Locate every blood parasite and identify its species.
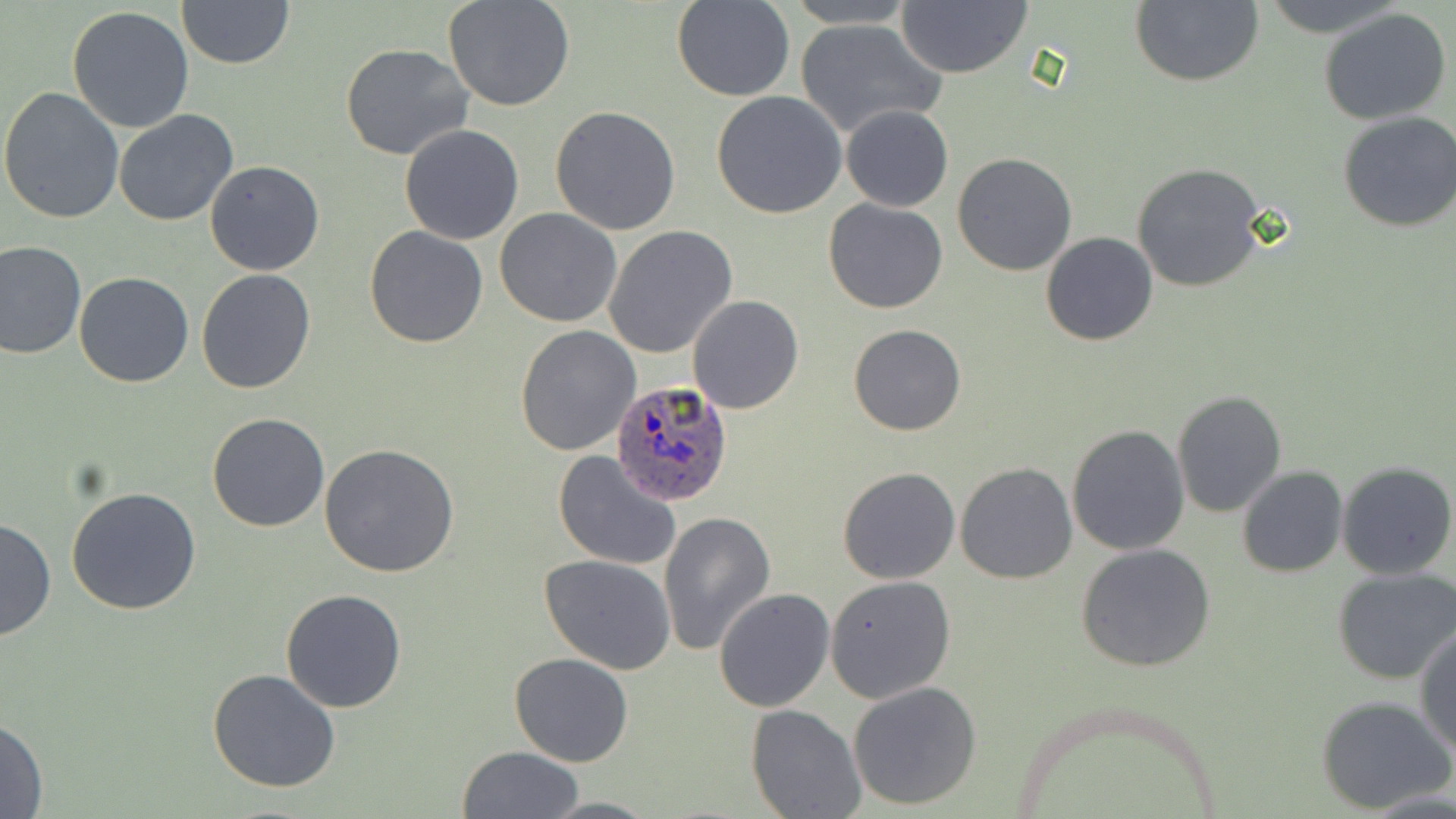

Approximate bounding boxes as (x1, y1, x2, y2) in pixels.
Plasmodium ovale-infected red blood cells: (610, 381, 732, 507).
No Plasmodium falciparum, Plasmodium malariae, Plasmodium vivax, Babesia divergens, or Trypanosoma brucei observed.

slide_level_diagnosis: Plasmodium ovale
magnification: 1000x
preparation: thin blood smear
image_size: 1456×819 pixels
modality: optical microscopy
stain: May-Grünwald-Giemsa
field_of_view: single
uninfected_red_blood_cell_locations: 'approximate bounding boxes as (x1, y1, x2, y2) in pixels: (176, 0, 293, 69), (443, 0, 576, 112), (672, 0, 795, 102), (1129, 0, 1263, 88), (1257, 0, 1411, 36), (783, 1, 917, 28), (898, 2, 1031, 78), (67, 6, 196, 134), (1319, 7, 1450, 124), (795, 18, 946, 139), (338, 43, 476, 162), (0, 87, 125, 226), (712, 91, 847, 218), (841, 104, 952, 212), (550, 105, 681, 235), (114, 109, 238, 226), (1337, 110, 1456, 232), (399, 124, 525, 244), (952, 153, 1078, 275), (205, 160, 324, 275), (1130, 163, 1268, 292), (825, 199, 947, 314), (495, 209, 622, 328), (603, 226, 738, 360), (365, 227, 489, 348), (1040, 232, 1159, 345), (0, 241, 86, 359), (195, 268, 317, 395), (73, 271, 194, 388), (688, 294, 804, 415), (848, 323, 967, 436), (514, 325, 640, 456), (1171, 391, 1286, 518), (208, 413, 329, 532), (1066, 424, 1189, 556), (318, 444, 462, 578), (552, 449, 683, 571), (954, 461, 1078, 584), (1335, 461, 1456, 580), (1236, 465, 1348, 578), (838, 466, 962, 585), (66, 485, 201, 616), (658, 510, 775, 656), (0, 517, 55, 642), (1076, 544, 1216, 671), (539, 554, 675, 675), (1332, 567, 1456, 684), (825, 575, 956, 704), (281, 589, 408, 713), (714, 590, 835, 712), (1415, 625, 1455, 757), (509, 654, 635, 767), (209, 667, 342, 792), (848, 682, 981, 811), (1315, 694, 1453, 814), (746, 703, 867, 819), (0, 715, 49, 819), (456, 746, 584, 819), (539, 795, 657, 817)'